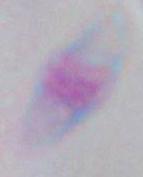
Photomicrograph. 1000x magnification. Toxoplasma gondii is seen.